Report the malaria status of this cell.
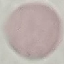

Uninfected.

Photographed with a smartphone camera at the microscope eyepiece. Giemsa stain. Cell patch, automatically extracted from a larger field of view and resized to 64 × 64 pixels. Thin smear of blood.